Report the malaria status of this cell.
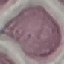
It is uninfected.

Acquired by smartphone through the microscope eyepiece. Giemsa stain. Automatically extracted cell patch, resized to 64 × 64 pixels. Thin smear of blood.